State the blood parasite species.
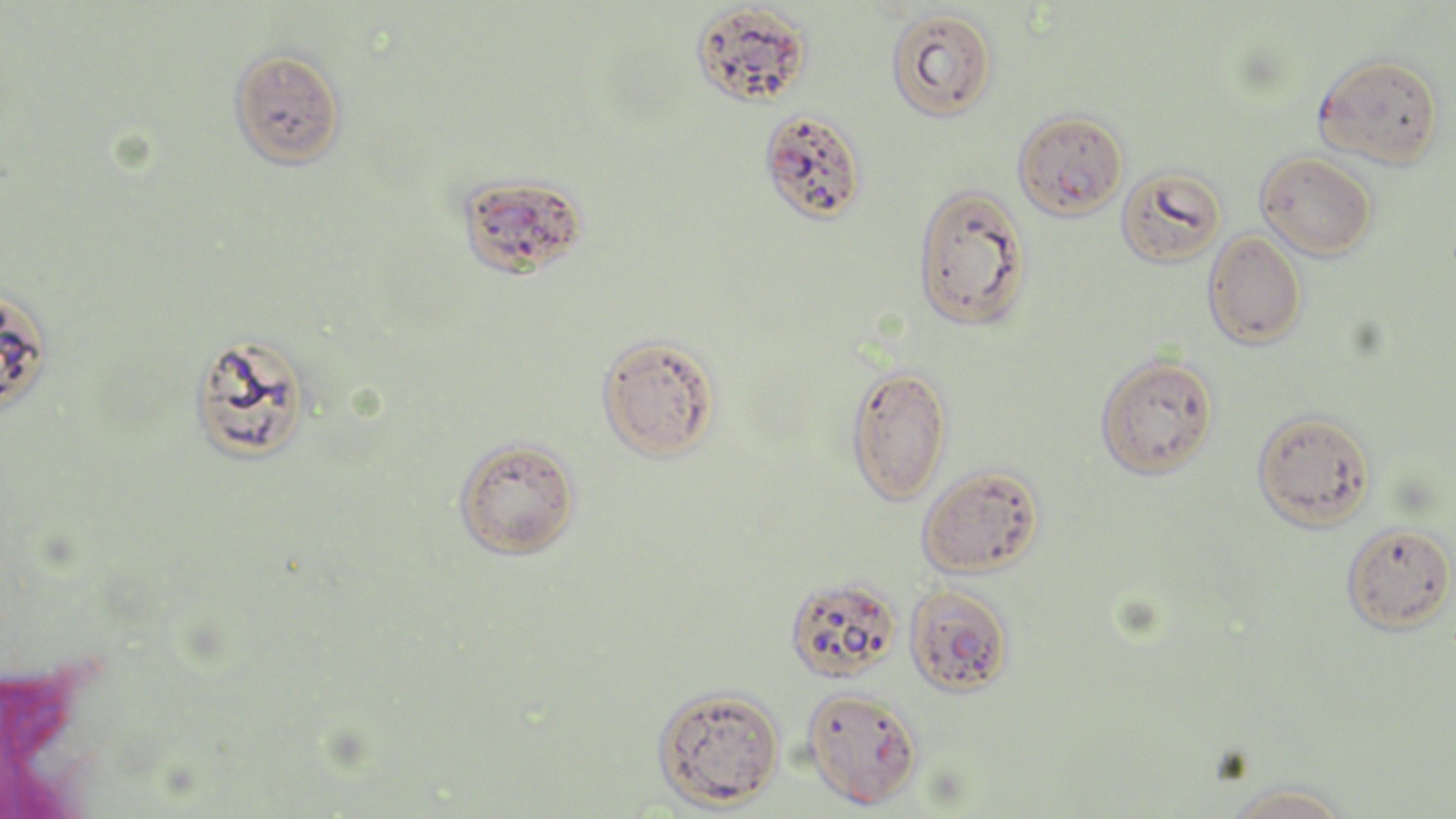

Plasmodium falciparum.

uninfected_red_blood_cell_locations: 'approximate bounding boxes as (x1,y1)-(x2,y2) corner pairs in pixels: (690,2)-(812,108), (885,7)-(998,122), (227,47)-(346,170), (1313,53)-(1444,169), (1012,110)-(1128,220), (1256,151)-(1378,261), (1116,165)-(1227,268), (454,172)-(588,280), (912,183)-(1031,331), (1202,230)-(1307,349), (0,287)-(54,415), (187,332)-(313,466), (596,334)-(721,462), (1095,354)-(1219,479), (845,364)-(952,505), (1252,410)-(1377,531), (453,437)-(582,560), (916,464)-(1045,578), (1341,522)-(1455,634), (783,576)-(901,683), (903,584)-(1013,697), (651,684)-(785,809), (801,687)-(922,810), (1222,780)-(1355,818)'
field_of_view: one of a larger specimen
preparation: thin blood film
stain: May-Grünwald-Giemsa
image_size: 1456×819 pixels
magnification: 1000x
modality: light microscopy
plasmodium_falciparum_infected_red_blood_cell_locations: 'approximate bounding boxes as (x1,y1)-(x2,y2) corner pairs in pixels: (757,109)-(867,225)'